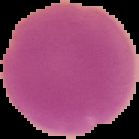

Summary:
  - Image size: 139×139 pixels
  - Image type: segmented cell region with the area outside set to black
  - Preparation: thin blood film
  - Result: no malaria parasites detected